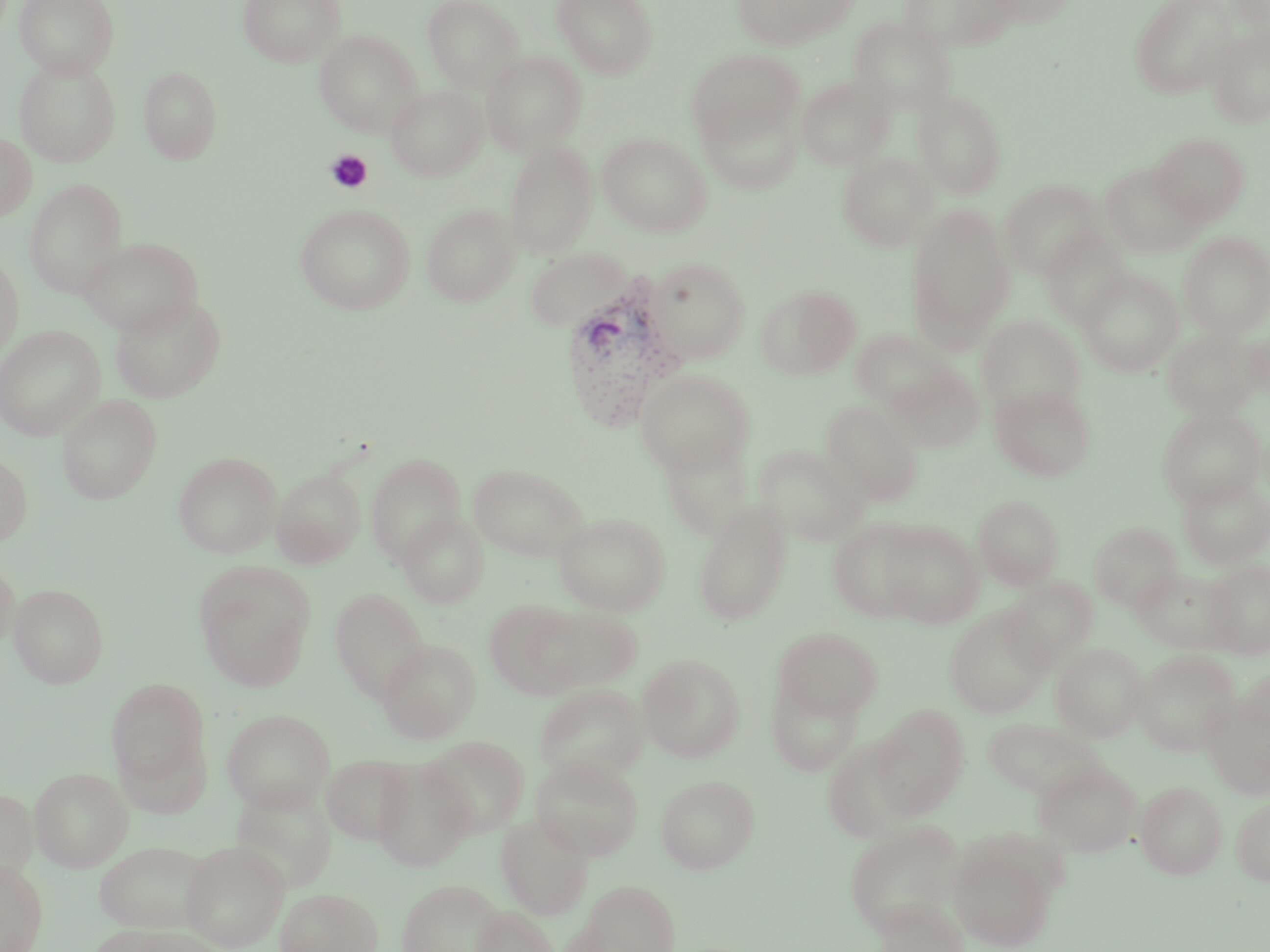
Summary:
  - Coordinate format: approximate bounding boxes as (x1,y1)-(x2,y2) corner pairs in pixels
  - Uninfected red blood cell locations: (14,0)-(118,79), (237,0)-(346,66), (421,0)-(524,91), (551,0)-(657,79), (732,0)-(852,50), (900,0)-(1018,52), (985,0)-(1076,29), (1129,0)-(1234,98), (1228,0)-(1270,40), (850,16)-(957,115), (1208,26)-(1270,127), (314,30)-(423,136), (688,49)-(803,149), (482,51)-(587,155), (14,58)-(120,166), (139,66)-(223,164), (796,74)-(894,170), (386,85)-(487,181), (912,89)-(1008,199), (698,100)-(802,195), (0,132)-(37,221), (1150,132)-(1250,225), (597,133)-(712,236), (504,141)-(598,259), (837,151)-(937,251), (1100,161)-(1205,258), (24,179)-(128,297), (1001,179)-(1102,279), (294,203)-(415,315), (421,204)-(521,306), (904,204)-(1015,351), (1039,228)-(1131,327), (1179,231)-(1270,337), (77,236)-(203,335), (524,247)-(632,332), (0,253)-(24,360), (646,257)-(750,364), (1077,269)-(1183,377), (756,285)-(860,380), (110,293)-(227,402), (978,315)-(1085,416), (0,325)-(105,440), (1247,327)-(1270,403), (1162,328)-(1262,418), (850,329)-(947,412), (894,364)-(985,451), (635,369)-(754,474), (990,384)-(1095,481), (56,394)-(162,504), (821,400)-(923,505), (1157,406)-(1266,508), (659,432)-(755,541), (754,444)-(867,545), (173,452)-(281,558), (0,454)-(33,546), (366,454)-(467,564), (467,463)-(588,562), (272,469)-(365,566), (1176,473)-(1270,569), (973,495)-(1063,589), (692,500)-(792,625), (397,512)-(489,608), (552,512)-(671,615), (826,518)-(927,622), (876,520)-(984,627), (1089,521)-(1183,612), (0,559)-(21,652), (1203,559)-(1270,659), (194,562)-(316,690), (1131,567)-(1237,654), (1001,577)-(1097,668), (9,583)-(109,688), (330,588)-(429,701), (485,600)-(588,700), (534,606)-(643,691), (944,606)-(1052,718), (773,627)-(882,721), (377,640)-(481,742), (1051,642)-(1148,741), (1132,649)-(1242,756), (638,654)-(745,762), (1239,668)-(1270,752), (766,674)-(864,776), (106,677)-(211,794), (533,684)-(647,784), (1201,692)-(1270,799), (872,704)-(969,820), (222,709)-(335,813), (983,718)-(1103,799), (822,734)-(920,843), (421,736)-(530,837), (323,754)-(415,844), (531,756)-(642,860), (371,757)-(473,871), (1033,759)-(1142,856), (31,767)-(133,871), (655,774)-(760,873), (1135,781)-(1227,879), (229,782)-(337,893), (0,788)-(38,883), (1231,796)-(1270,886), (497,813)-(593,919), (844,820)-(967,938), (947,829)-(1064,950), (95,841)-(212,933), (180,841)-(289,951), (0,860)-(48,952), (397,879)-(506,952), (572,880)-(680,952), (275,887)-(382,952), (873,898)-(967,952), (470,905)-(558,952), (91,924)-(215,951)
  - Plasmodium vivax-infected red blood cell locations: (558,279)-(684,432)
  - Platelet locations: (325,149)-(373,193)
  - Slide-level diagnosis: Plasmodium vivax
  - Preparation: thin blood smear
  - Magnification: 1000x
  - Modality: optical microscopy
  - Image size: 1270×952 pixels
  - Stain: May-Grünwald-Giemsa
  - Field of view: single